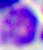
A leukocyte is shown. Micrograph. 400x magnification.